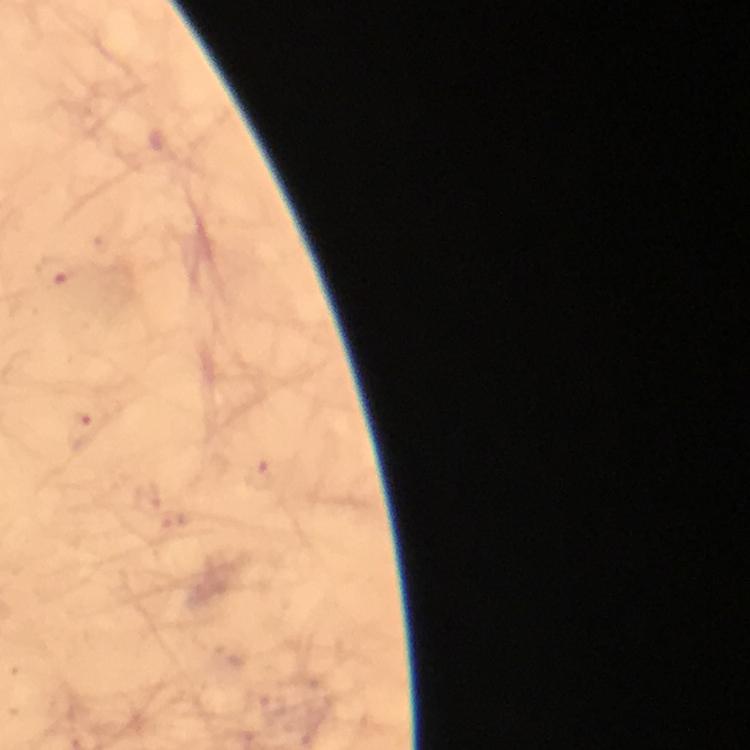
Approximate centers as [x, y] in pixels.
Summary:
  - Plasmodium parasite locations: [57, 273], [83, 432]
  - Preparation: thick blood film
  - Context: from a malaria diagnostic workup
  - Cropped from: one field of view
  - Image size: 750×750 pixels
  - Capture: smartphone photograph through a microscope
  - Stain: Giemsa
  - Immersion oil: used
  - Magnification: 100x